Name the parasite shown.
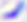

This is Toxoplasma gondii.

{
  "magnification": "400x",
  "modality": "photomicrograph"
}